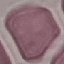
malaria status = uninfected
preparation = thin blood smear
capture = smartphone through the microscope eyepiece
image type = automatically extracted cell patch, resized to 64 × 64 pixels
stain = Giemsa